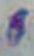
identification: Toxoplasma gondii
magnification: 1000x
modality: micrograph